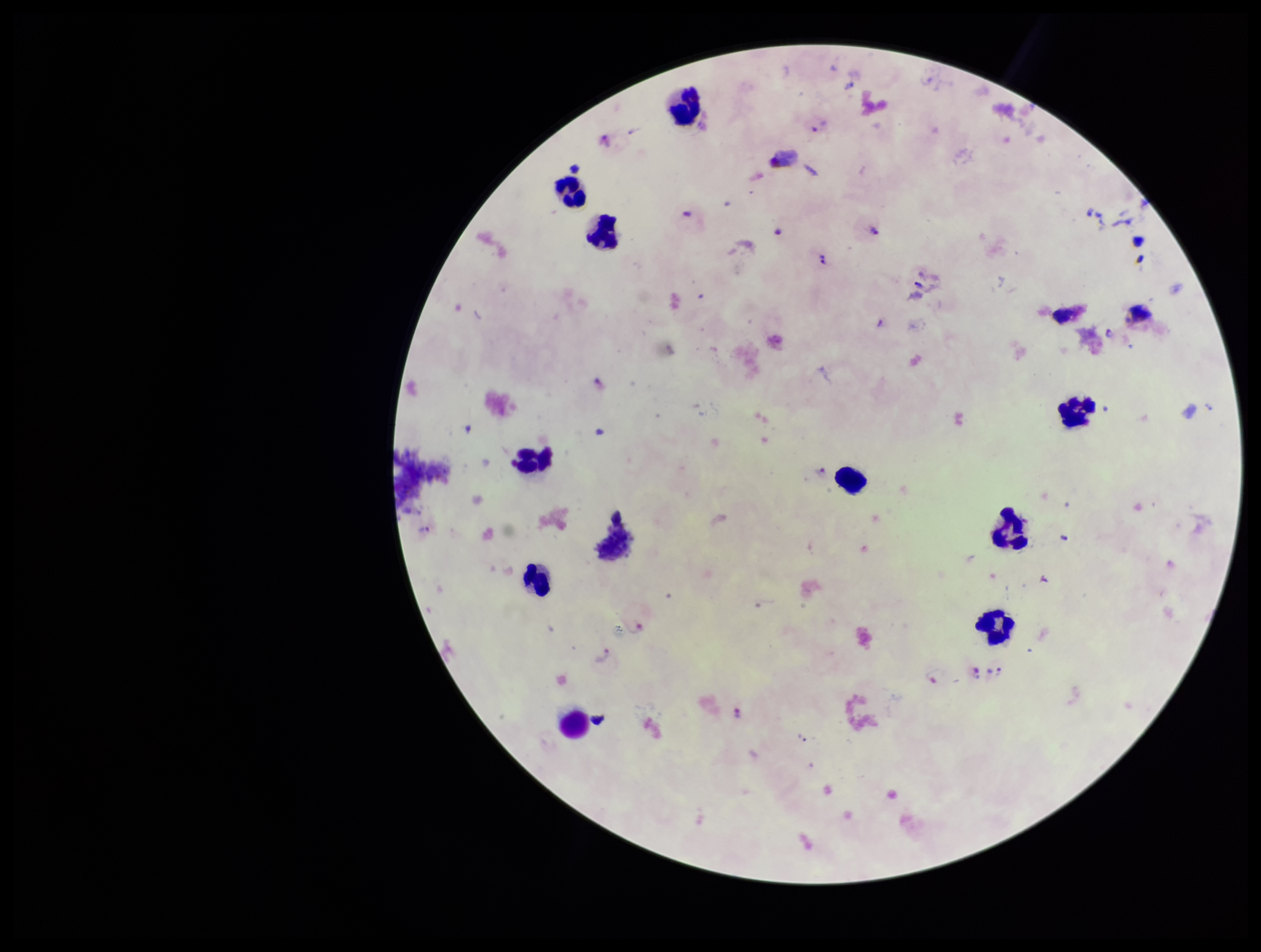

{
  "patient_malaria_status": "positive",
  "preparation": "thick smear",
  "species_reported_for_this_patient": "Plasmodium vivax",
  "plasmodium_parasites": "detected",
  "capture": "smartphone photograph through the microscope eyepiece",
  "parasite_count": 14,
  "stain": "Giemsa",
  "image_size": "1261×952 pixels",
  "leukocyte_count": 13,
  "field_of_view": "single"
}